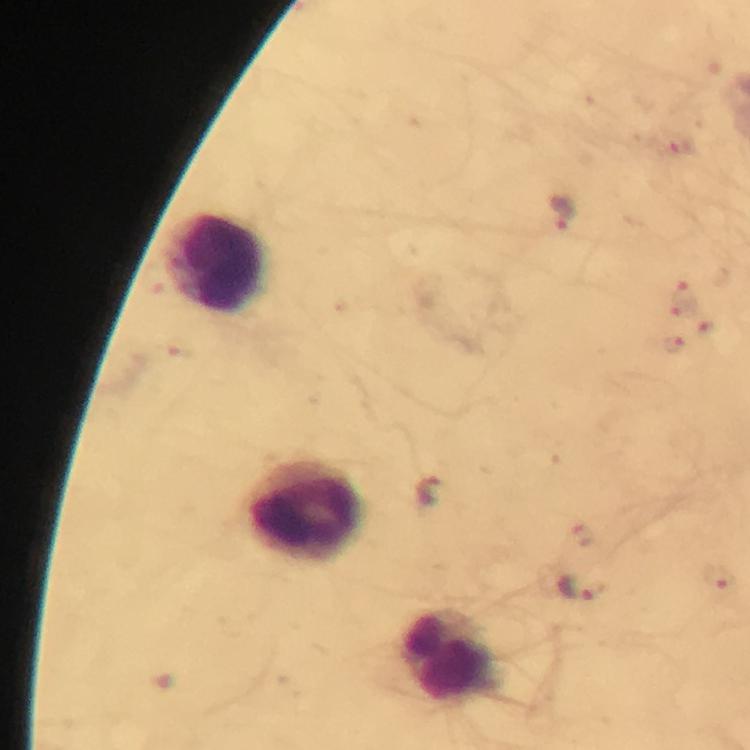

Approximate centers as {x, y} in pixels. Leukocyte locations: {216, 264}, {303, 511}, {450, 657}. Malaria parasite locations: {563, 212}, {429, 490}, {721, 581}, {585, 587}. Immersion oil applied. From a diagnostic examination for malaria. 100x magnification. Image is 750×750 pixels. Thick blood film. Giemsa-stained preparation. A crop from one field of view. Smartphone photograph taken through a microscope.